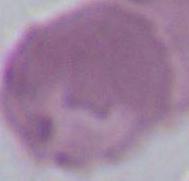
Summary:
  - Identification: red blood cell
  - Modality: micrograph
  - Magnification: 1000x